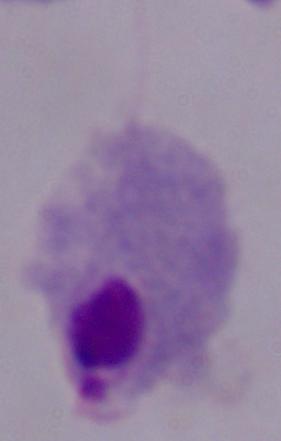

modality = micrograph
magnification = 1000x
identification = trichomonad